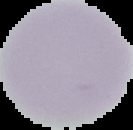
{
  "result": "no malaria parasites seen",
  "image_type": "segmented cell region on a black background",
  "preparation": "thin blood film",
  "image_size": "133×130 pixels"
}